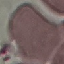 Malaria status: uninfected. Giemsa stain. Acquired by smartphone through the microscope eyepiece. Thin smear of blood. Cell patch, automatically extracted from a larger field of view and resized to 64 × 64 pixels.